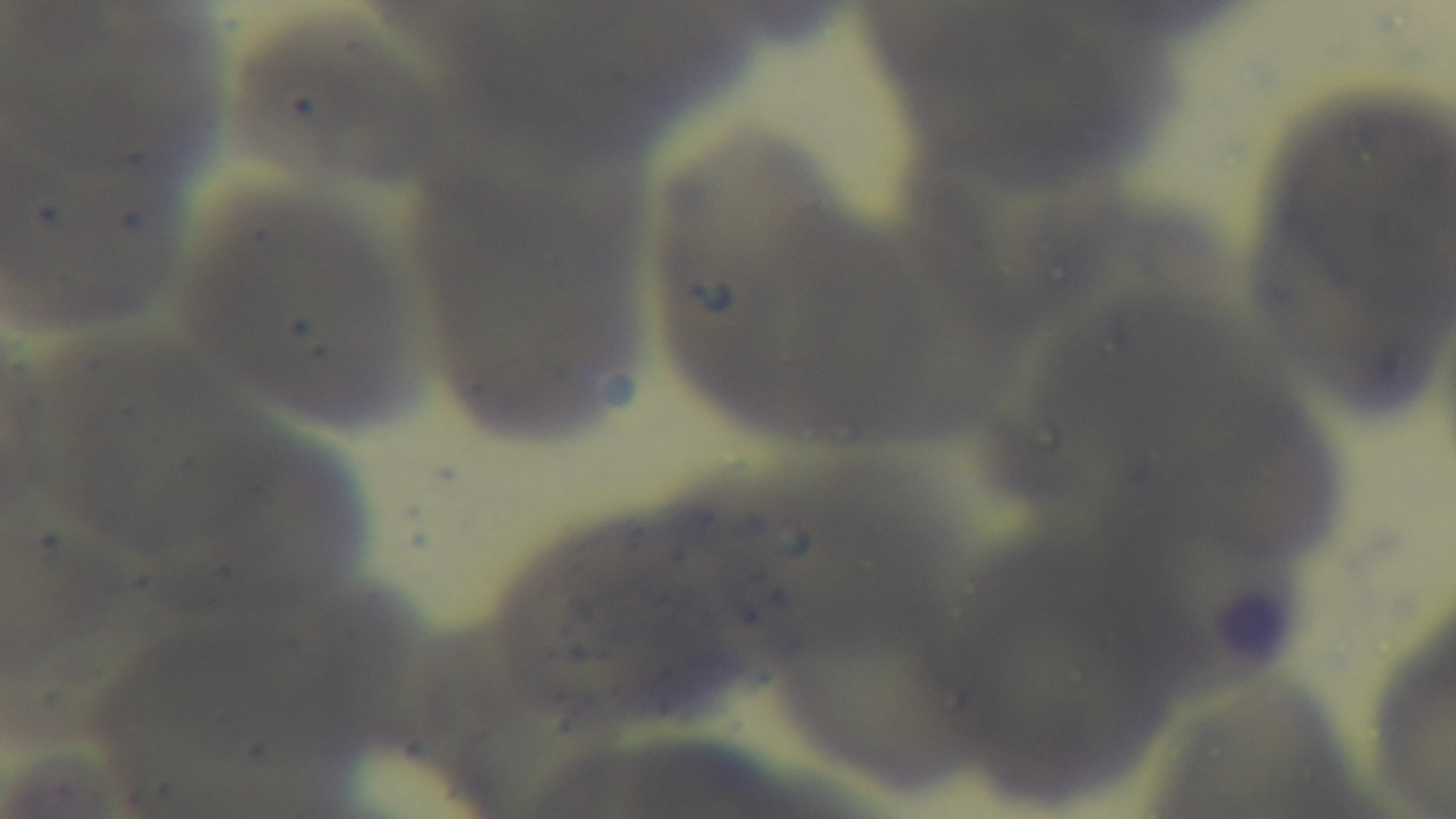 One field from the slide. Preparation: thin smear. Oil-immersion objective, 100x. Malaria status: uninfected. Photomicrograph. Giemsa-stained. Captured with a mounted 4K digital camera.